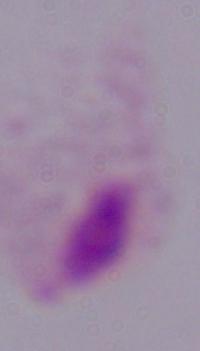

Summary:
  - Identification: trichomonad
  - Magnification: 1000x
  - Modality: photomicrograph